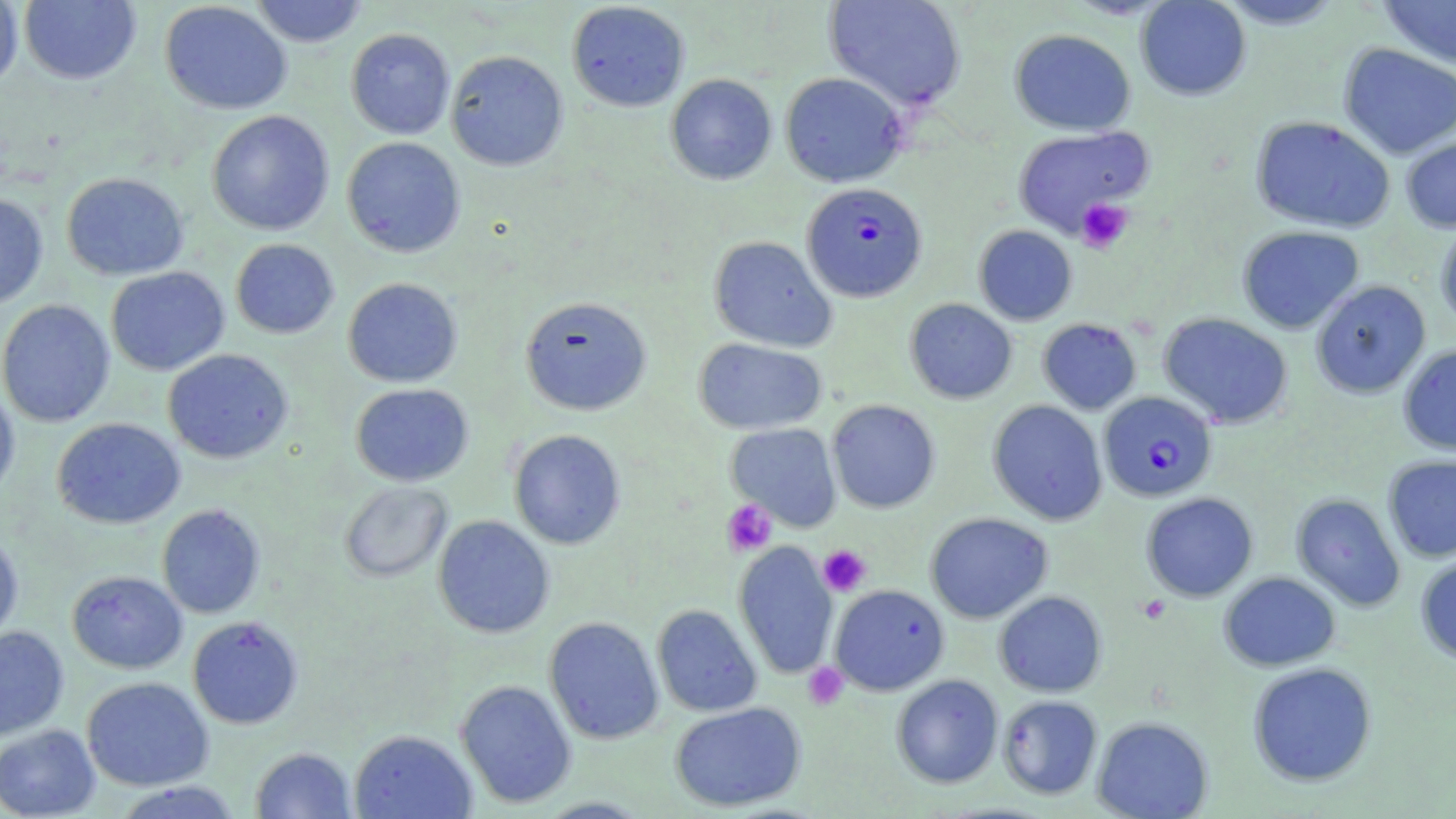
Summary:
  - Coordinate format: approximate bounding boxes as [x1, y1, x2, y2] in pixels
  - Plasmodium falciparum-infected red blood cell locations: [802, 182, 927, 302], [1098, 391, 1217, 501]
  - Uninfected red blood cell locations: [19, 0, 141, 85], [249, 0, 368, 47], [823, 0, 967, 111], [1135, 0, 1252, 101], [1212, 0, 1348, 29], [1379, 0, 1456, 68], [0, 1, 23, 91], [159, 1, 292, 115], [566, 1, 690, 112], [345, 28, 455, 140], [1009, 28, 1136, 135], [1338, 43, 1456, 160], [446, 50, 568, 171], [780, 72, 907, 188], [665, 73, 777, 185], [207, 110, 334, 236], [1250, 115, 1396, 234], [1012, 126, 1151, 236], [1401, 135, 1456, 233], [341, 137, 466, 257], [61, 172, 188, 280], [0, 192, 49, 309], [1435, 220, 1456, 331], [974, 225, 1077, 325], [1237, 225, 1364, 333], [709, 235, 836, 352], [230, 238, 339, 339], [105, 267, 230, 376], [342, 277, 462, 387], [1310, 280, 1431, 399], [520, 295, 652, 415], [905, 298, 1017, 403], [0, 299, 116, 428], [1158, 312, 1293, 428], [1038, 318, 1141, 414], [694, 338, 826, 435], [1397, 344, 1456, 455], [162, 348, 293, 464], [350, 383, 473, 487], [0, 384, 20, 504], [827, 399, 941, 513], [987, 400, 1108, 525], [51, 417, 185, 529], [725, 422, 842, 531], [508, 429, 626, 549], [1383, 455, 1456, 563], [339, 481, 452, 583], [1141, 492, 1258, 602], [1291, 493, 1405, 612], [157, 504, 265, 619], [925, 512, 1053, 624], [432, 515, 555, 638], [0, 532, 23, 645], [733, 541, 838, 680], [1414, 552, 1456, 665], [67, 570, 187, 674], [1218, 571, 1341, 671], [829, 584, 949, 696], [993, 590, 1107, 697], [652, 604, 762, 717], [187, 615, 303, 729], [544, 616, 664, 745], [0, 625, 69, 740], [1247, 661, 1377, 787], [891, 674, 1004, 789], [81, 677, 213, 791], [455, 680, 577, 808], [997, 695, 1102, 799], [669, 701, 806, 811], [1091, 716, 1213, 818], [0, 724, 101, 818], [349, 729, 477, 819], [250, 746, 356, 818], [111, 780, 244, 818], [532, 796, 654, 818]
  - Platelet locations: [1075, 199, 1133, 253], [721, 499, 777, 556], [818, 545, 872, 597], [1137, 595, 1171, 624], [803, 663, 847, 710]
  - Slide-level diagnosis: Plasmodium falciparum
  - Field of view: one of a larger specimen
  - Magnification: 1000x
  - Stain: May-Grünwald-Giemsa
  - Modality: optical microscopy
  - Preparation: thin blood film
  - Image size: 1456×819 pixels